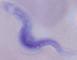
Summary:
  - Identification: trypanosome
  - Modality: micrograph
  - Magnification: 1000x